Report the malaria status of this cell.
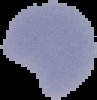
It is parasitized.

{
  "preparation": "thin blood film",
  "image_size": "97×100 pixels",
  "image_type": "cell region segmented out of the field of view; surrounding area masked to black"
}